Report the malaria status of this cell.
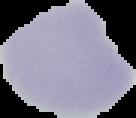
It is uninfected.

From a thin blood film. Segmented cell region on a black background. Image is 136×118 pixels.